Report the malaria status of this cell.
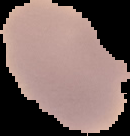

Uninfected.

Image is 130×136 pixels. The area outside the segmented cell region is set to black. From a thin blood smear.